Identify the blood parasite species.
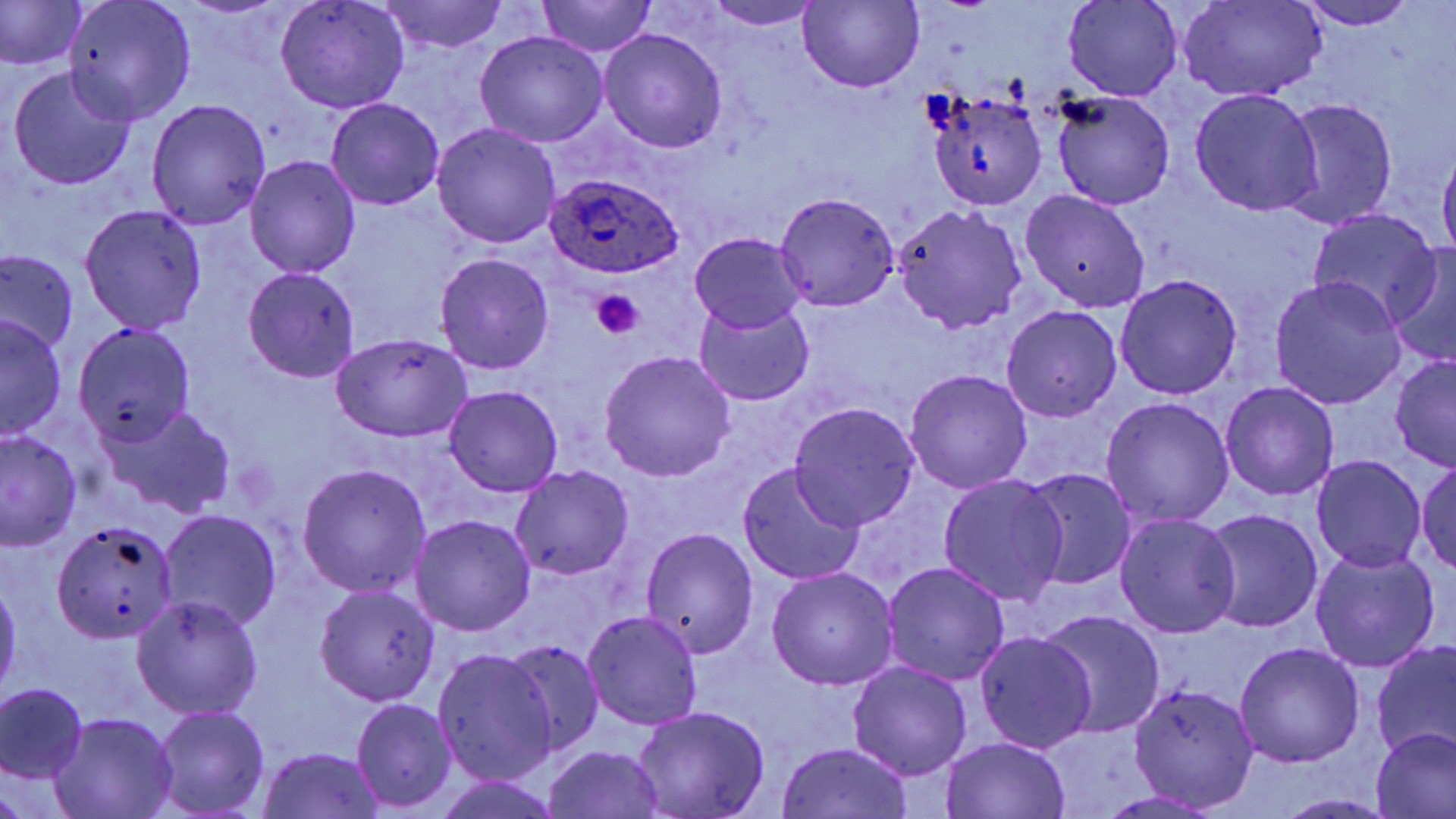
Plasmodium ovale.

Approximate bounding boxes as [x1, y1, x2, y2] in pixels. Platelet locations: [591, 291, 645, 338]. Plasmodium ovale-infected red blood cell locations: [544, 173, 684, 279]. Uninfected red blood cell locations: [275, 0, 408, 112], [377, 0, 510, 55], [701, 0, 824, 30], [798, 0, 925, 92], [1179, 0, 1327, 102], [1293, 0, 1422, 30], [0, 1, 86, 68], [64, 1, 198, 124], [535, 1, 658, 58], [1064, 1, 1182, 102], [599, 29, 728, 154], [474, 31, 608, 148], [8, 66, 138, 190], [1188, 89, 1322, 217], [1052, 90, 1175, 210], [928, 92, 1046, 211], [1280, 98, 1399, 229], [147, 99, 272, 230], [326, 99, 445, 209], [431, 122, 562, 249], [1438, 147, 1456, 265], [244, 155, 360, 280], [1020, 188, 1151, 314], [775, 192, 900, 312], [80, 205, 208, 333], [894, 205, 1027, 333], [1306, 210, 1443, 327], [690, 233, 806, 332], [1385, 247, 1456, 366], [1, 249, 78, 353], [435, 252, 555, 375], [241, 268, 361, 384], [1115, 274, 1243, 399], [1269, 276, 1405, 410], [694, 300, 815, 405], [1000, 305, 1121, 424], [0, 315, 66, 439], [72, 322, 193, 447], [332, 331, 473, 443], [597, 351, 737, 482], [1390, 354, 1455, 469], [904, 368, 1033, 494], [1220, 381, 1339, 503], [443, 385, 564, 498], [1101, 397, 1235, 529], [789, 402, 919, 531], [106, 405, 234, 517], [1, 430, 80, 549], [1311, 455, 1427, 572], [1415, 460, 1455, 575], [297, 463, 432, 598], [737, 463, 867, 585], [510, 466, 635, 583], [1021, 468, 1137, 592], [937, 473, 1068, 606], [158, 508, 282, 633], [1203, 509, 1323, 634], [1115, 513, 1241, 638], [411, 514, 536, 636], [50, 522, 179, 643], [642, 528, 759, 659], [1310, 546, 1440, 672], [883, 562, 1010, 685], [766, 567, 899, 690], [0, 579, 21, 700], [313, 584, 442, 706], [131, 595, 263, 720], [1040, 609, 1166, 739], [583, 611, 703, 731], [974, 631, 1096, 754], [505, 638, 607, 756], [1371, 641, 1456, 763], [1234, 642, 1366, 767], [432, 648, 559, 786], [849, 662, 973, 781], [1129, 683, 1260, 809], [0, 684, 87, 784], [352, 700, 457, 811], [152, 705, 270, 817], [633, 706, 770, 818], [49, 712, 178, 819], [1371, 728, 1456, 819], [943, 736, 1070, 818], [775, 742, 915, 819], [543, 745, 667, 819], [257, 747, 384, 818], [1093, 791, 1229, 817], [1275, 793, 1400, 818]. May-Grünwald-Giemsa stain. Light microscopy. Captured at 1000x magnification. One field of a larger specimen. Image is 1456×819 pixels. Thin blood film.